Evaluate for Plasmodium parasites.
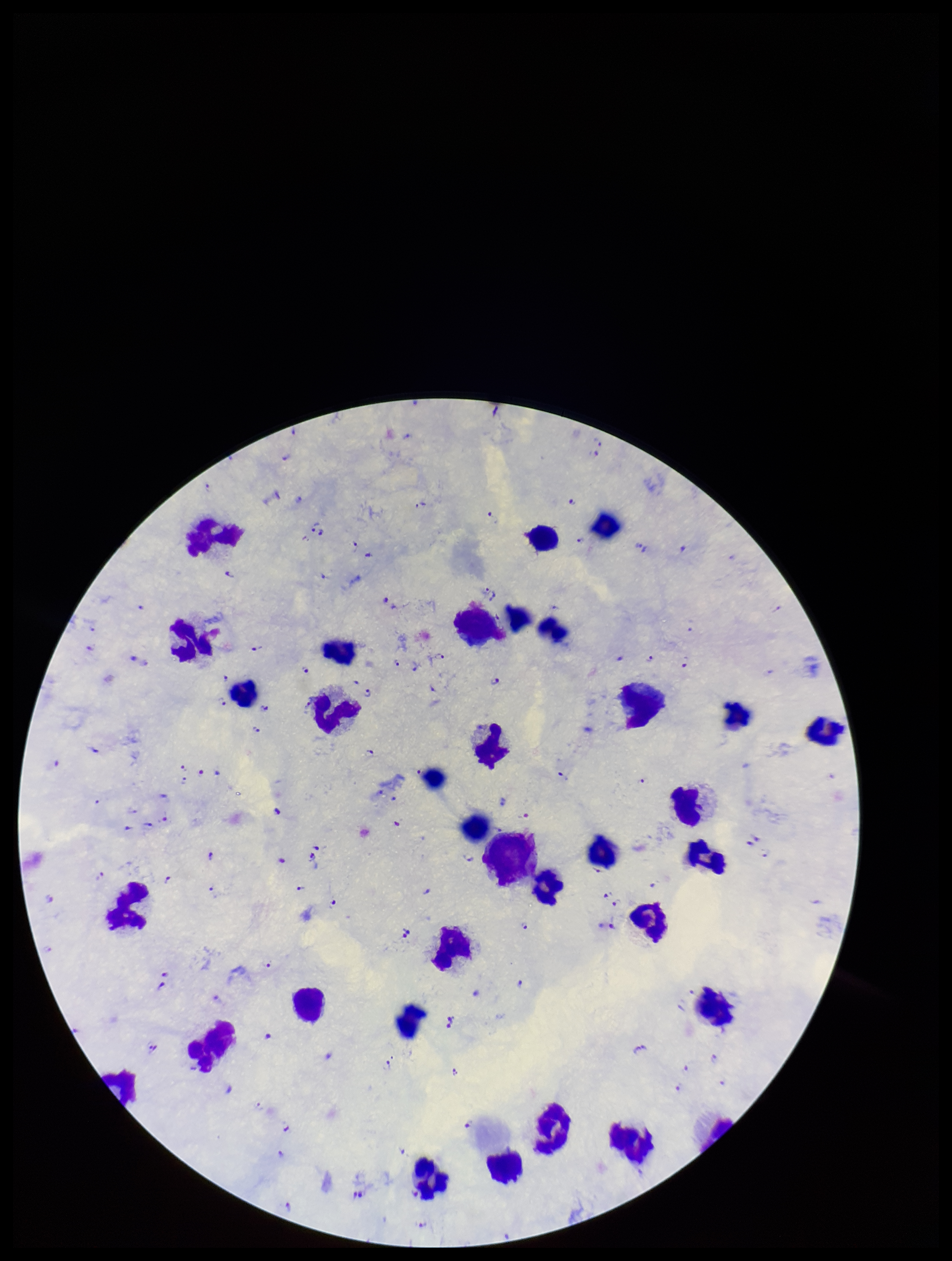

Detected.

leukocyte_count: 35
capture: smartphone photograph through the microscope eyepiece
patient_malaria_status: positive
preparation: thick
species_reported_for_this_patient: Plasmodium falciparum
stain: Giemsa
field_of_view: single
image_size: 952×1261 pixels
parasite_count: 108